Assess the morphology of the erythrocytes.
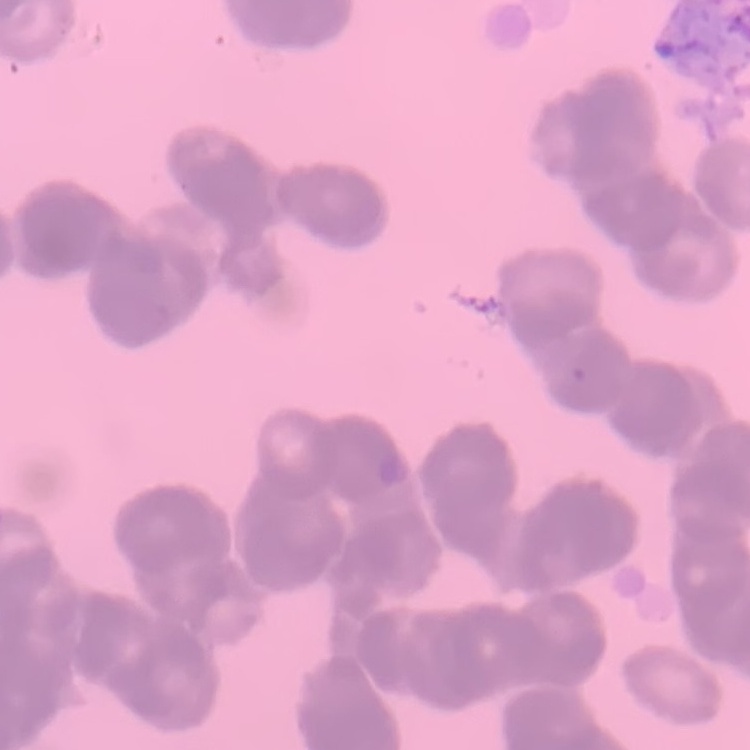

They show rouleaux formation.

{
  "image_type": "square crop of a larger photomicrograph",
  "stain": "Field's or Giemsa",
  "preparation": "thin peripheral smear"
}